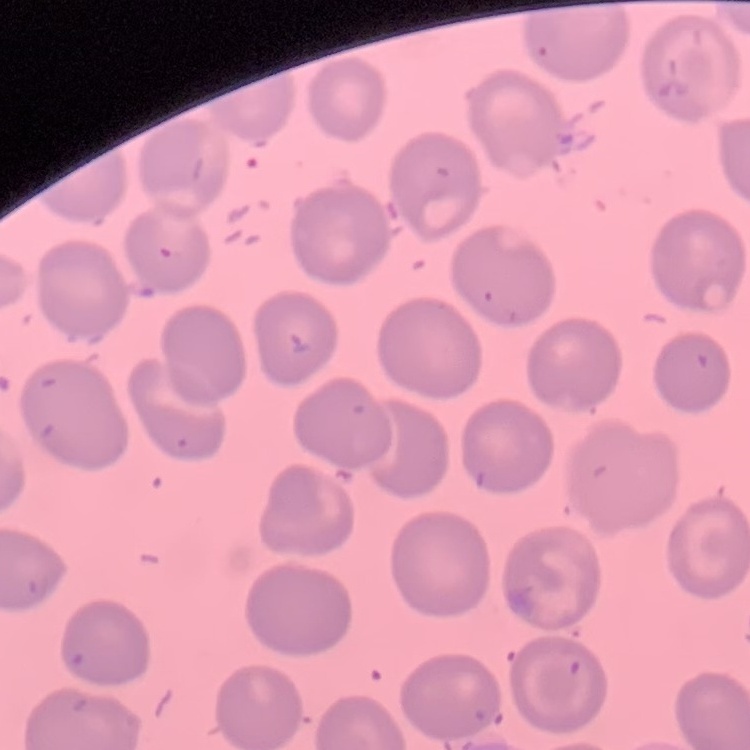
The red blood cells exhibit no rouleaux formation. Square crop of a larger photomicrograph. Thin peripheral smear. Field's or Giemsa stain.